Give the preparation type.
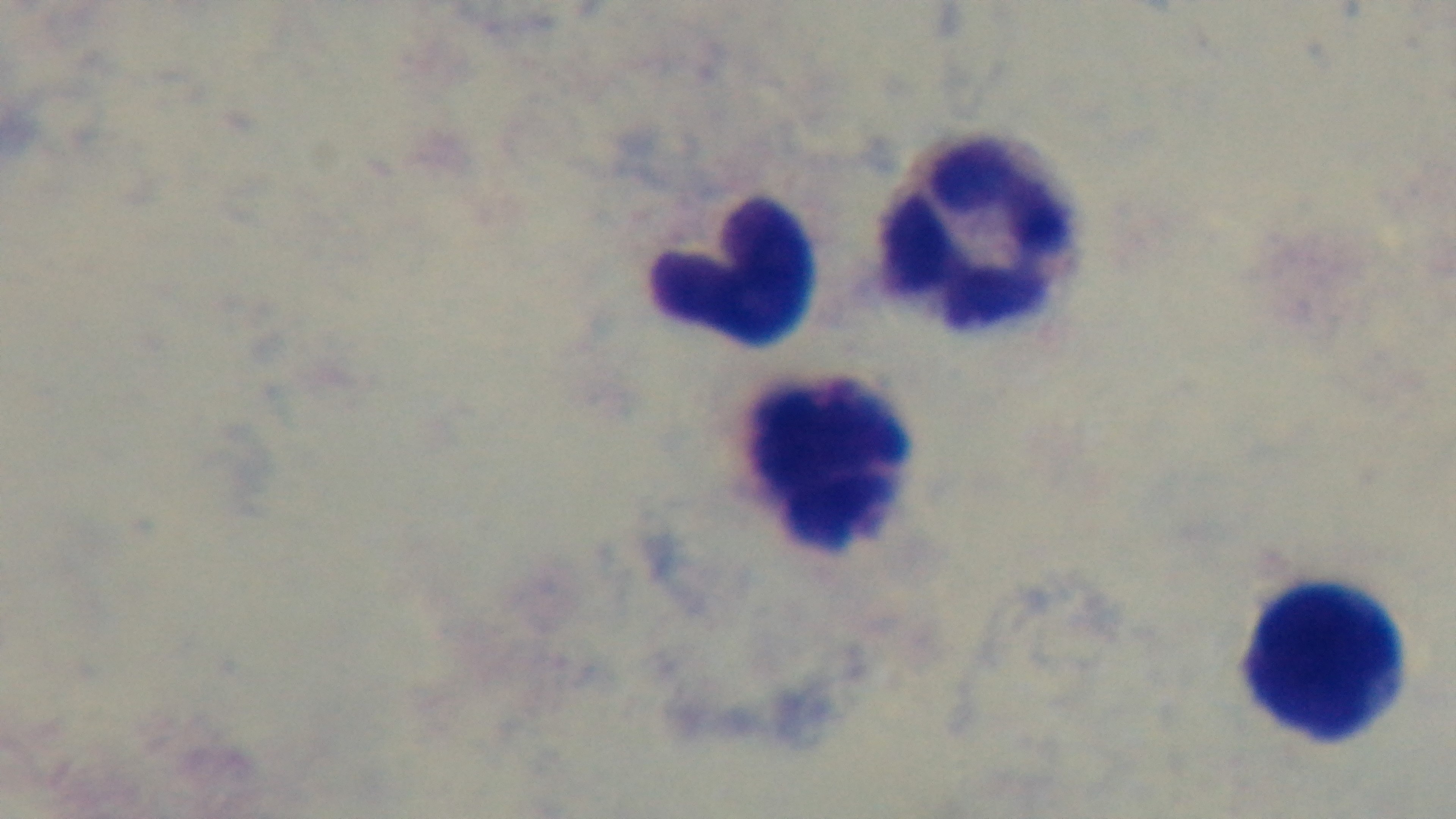
Thick.

Summary:
  - Field of view: one from the slide
  - Capture: mounted 4K digital camera
  - Malaria status: negative
  - Modality: light microscopy
  - Objective: 100x oil immersion
  - Stain: Giemsa